Outline each blood parasite and name the species.
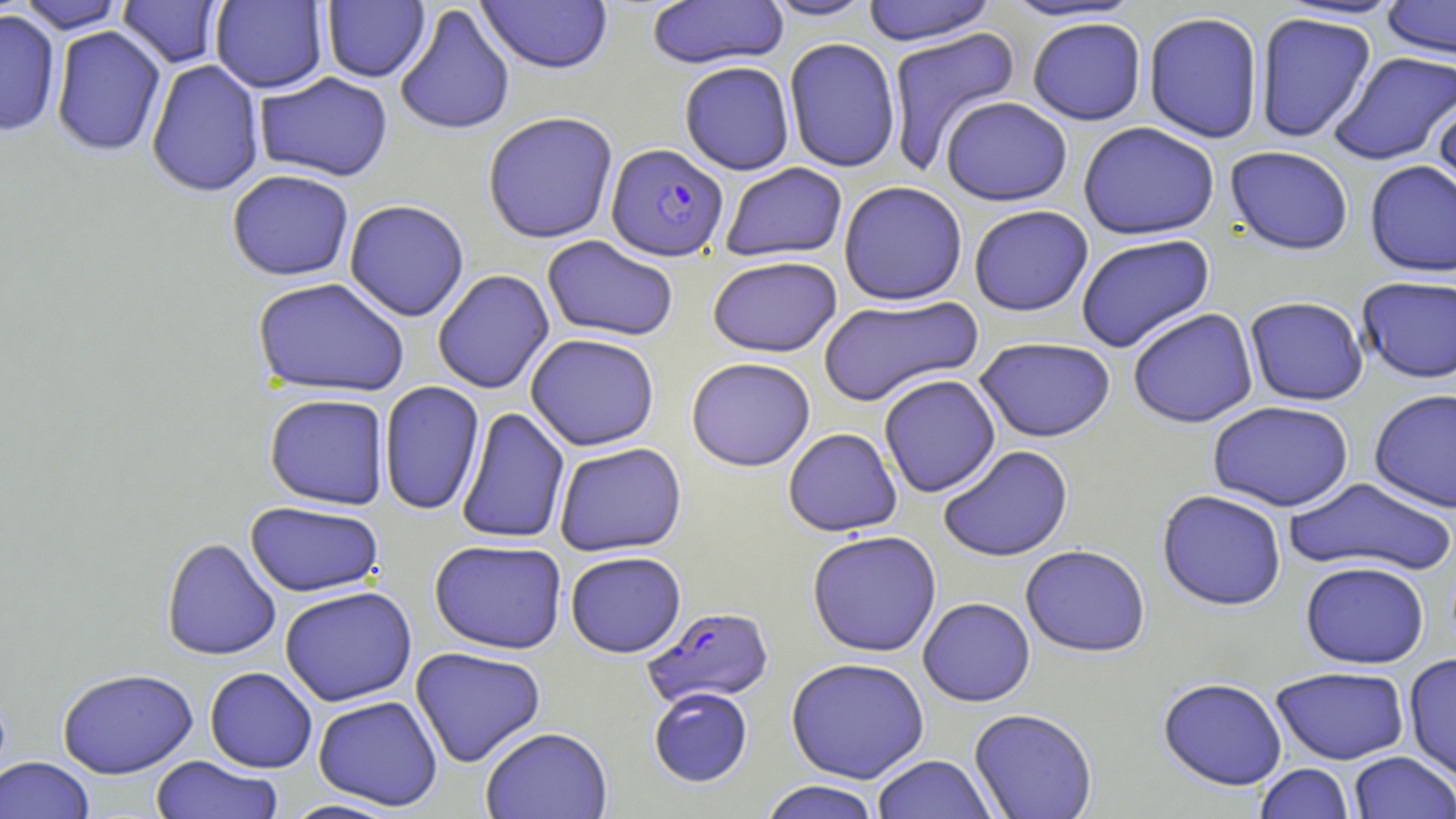

Approximate bounding boxes as (x1,y1)-(x2,y2) corner pairs in pixels.
Plasmodium falciparum-infected red blood cells: (606,144)-(729,262), (642,606)-(775,708).
No Plasmodium ovale, Plasmodium malariae, Plasmodium vivax, Babesia divergens, or Trypanosoma brucei observed.

Summary:
  - Uninfected red blood cell locations: (16,0)-(127,33), (646,0)-(789,72), (760,0)-(878,22), (1381,0)-(1456,61), (116,1)-(225,69), (210,1)-(328,94), (321,1)-(430,83), (476,1)-(613,76), (860,1)-(998,46), (996,1)-(1147,24), (393,4)-(516,137), (0,10)-(62,138), (1143,12)-(1263,145), (1255,13)-(1376,143), (1027,18)-(1147,127), (50,26)-(166,157), (885,27)-(1022,174), (784,39)-(901,174), (1329,51)-(1456,167), (146,59)-(265,198), (679,62)-(795,176), (254,72)-(394,182), (1432,95)-(1456,217), (940,97)-(1072,208), (482,112)-(619,245), (1078,123)-(1220,242), (1224,147)-(1353,258), (1364,161)-(1456,279), (721,163)-(848,263), (226,169)-(354,281), (838,182)-(968,307), (343,199)-(470,322), (969,206)-(1093,318), (541,235)-(679,343), (1076,235)-(1215,354), (707,257)-(842,359), (432,269)-(555,394), (252,277)-(410,398), (1357,277)-(1456,385), (818,294)-(984,408), (1244,298)-(1368,407), (1128,308)-(1258,429), (525,334)-(660,451), (974,338)-(1116,444), (686,357)-(816,472), (879,375)-(1001,498), (379,381)-(485,517), (1369,389)-(1456,514), (264,393)-(390,510), (1208,401)-(1354,512), (456,407)-(570,545), (783,428)-(903,537), (553,442)-(687,558), (938,445)-(1074,563), (1285,478)-(1455,577), (1156,490)-(1286,612), (244,501)-(385,597), (807,531)-(942,657), (160,537)-(282,661), (428,539)-(568,654), (1020,546)-(1151,659), (565,551)-(687,658), (1300,562)-(1430,670), (279,586)-(417,706), (918,598)-(1036,707), (410,646)-(546,767), (1403,654)-(1456,784), (785,658)-(930,784), (204,667)-(318,773), (1271,667)-(1410,766), (57,668)-(198,779), (1158,678)-(1287,792), (648,687)-(753,788), (313,695)-(443,811), (969,709)-(1097,819), (481,726)-(612,818), (1348,751)-(1456,819), (871,755)-(997,819), (150,756)-(283,819), (0,757)-(95,819), (1254,763)-(1355,819), (757,781)-(883,819), (278,798)-(406,818)
  - Slide-level diagnosis: Plasmodium falciparum
  - Magnification: 1000x
  - Field of view: single
  - Preparation: thin blood film
  - Stain: May-Grünwald-Giemsa
  - Modality: optical microscopy
  - Image size: 1456×819 pixels